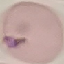

malaria_status: parasitized
stain: Giemsa
capture: smartphone camera at the microscope eyepiece
image_type: cell patch, automatically extracted from a larger field of view and resized to 64 × 64 pixels
preparation: thin blood smear